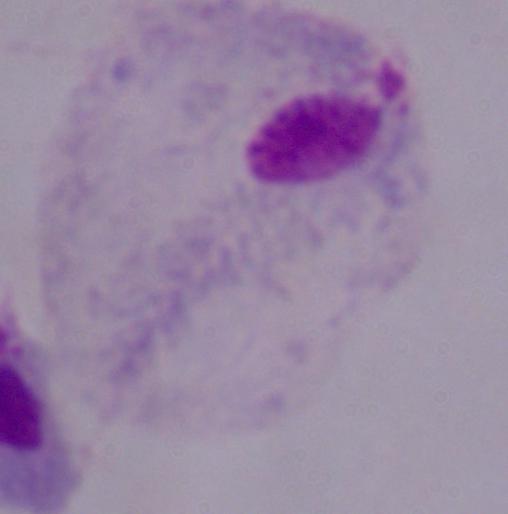
modality: photomicrograph
identification: trichomonad
magnification: 1000x